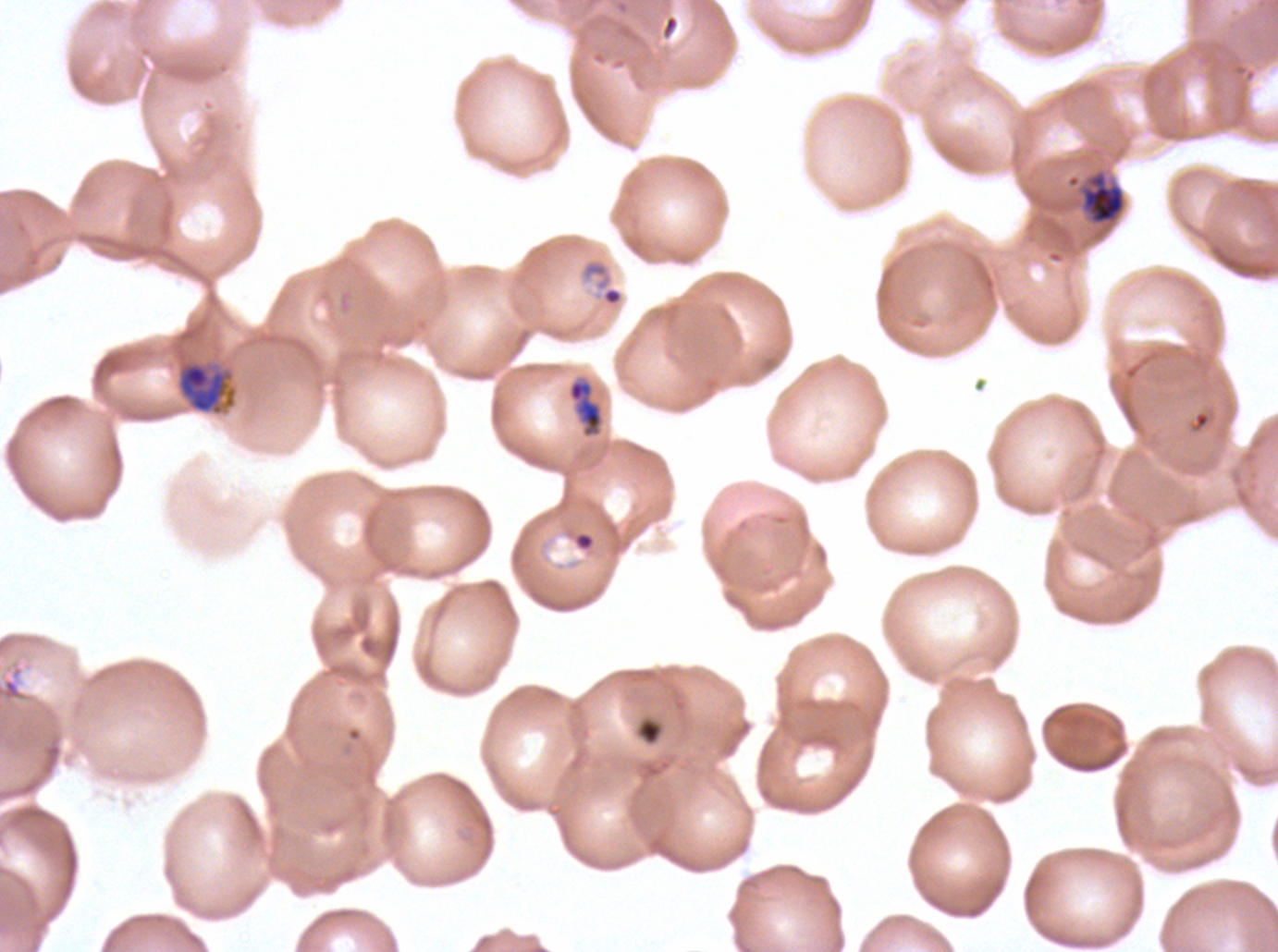
Approximate bounding boxes as (x1, y1, x2, y2) in pixels. Late-ring/early-trophozoite locations: (567, 379, 603, 438), (637, 718, 663, 745). Ring locations: (579, 258, 625, 309), (572, 531, 596, 552). Late trophozoite locations: (1080, 170, 1126, 226), (177, 360, 238, 416). Debris locations: (3, 677, 22, 701). Image is 1278×952 pixels. Plasmodium falciparum cultured ex vivo for 24 to 48 hours, from a patient in The Gambia. Giemsa-stained preparation. A sub-image separated from a larger composite. Life-cycle stages observed: ring, late-ring/early-trophozoite, late trophozoite. Thin blood film.